Name the parasite shown.
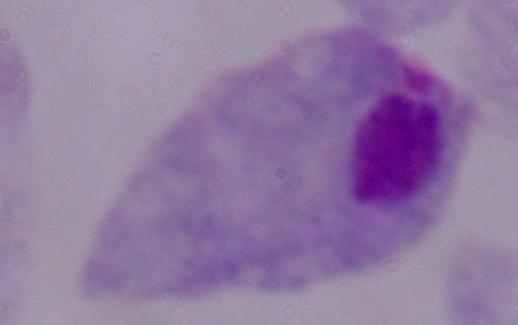
This is a trichomonad.

1000x magnification. Photomicrograph.